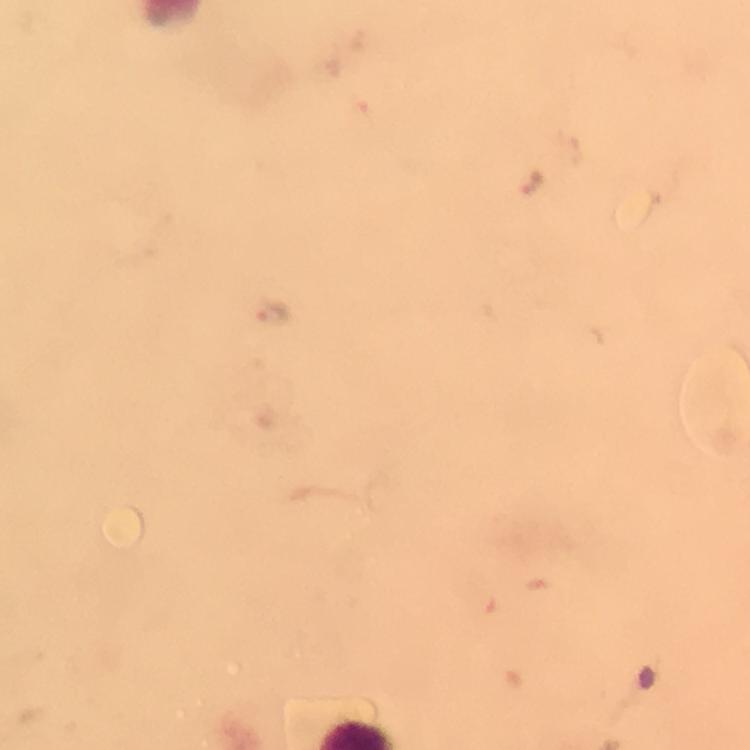

Approximate centers as [x, y] in pixels.
Summary:
  - Malaria parasite locations: [271, 313]
  - Immersion oil: applied
  - Stain: Giemsa
  - Cropped from: one field of view
  - Capture: smartphone mounted on the microscope
  - Image size: 750×750 pixels
  - Preparation: thick smear
  - Context: from a malaria diagnostic workup
  - Magnification: 100x